Assess this cell for malaria.
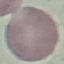
It is uninfected.

{
  "preparation": "thin blood film",
  "stain": "Giemsa",
  "capture": "smartphone through the microscope eyepiece",
  "image_type": "automatically extracted cell patch, resized to 64 × 64 pixels"
}